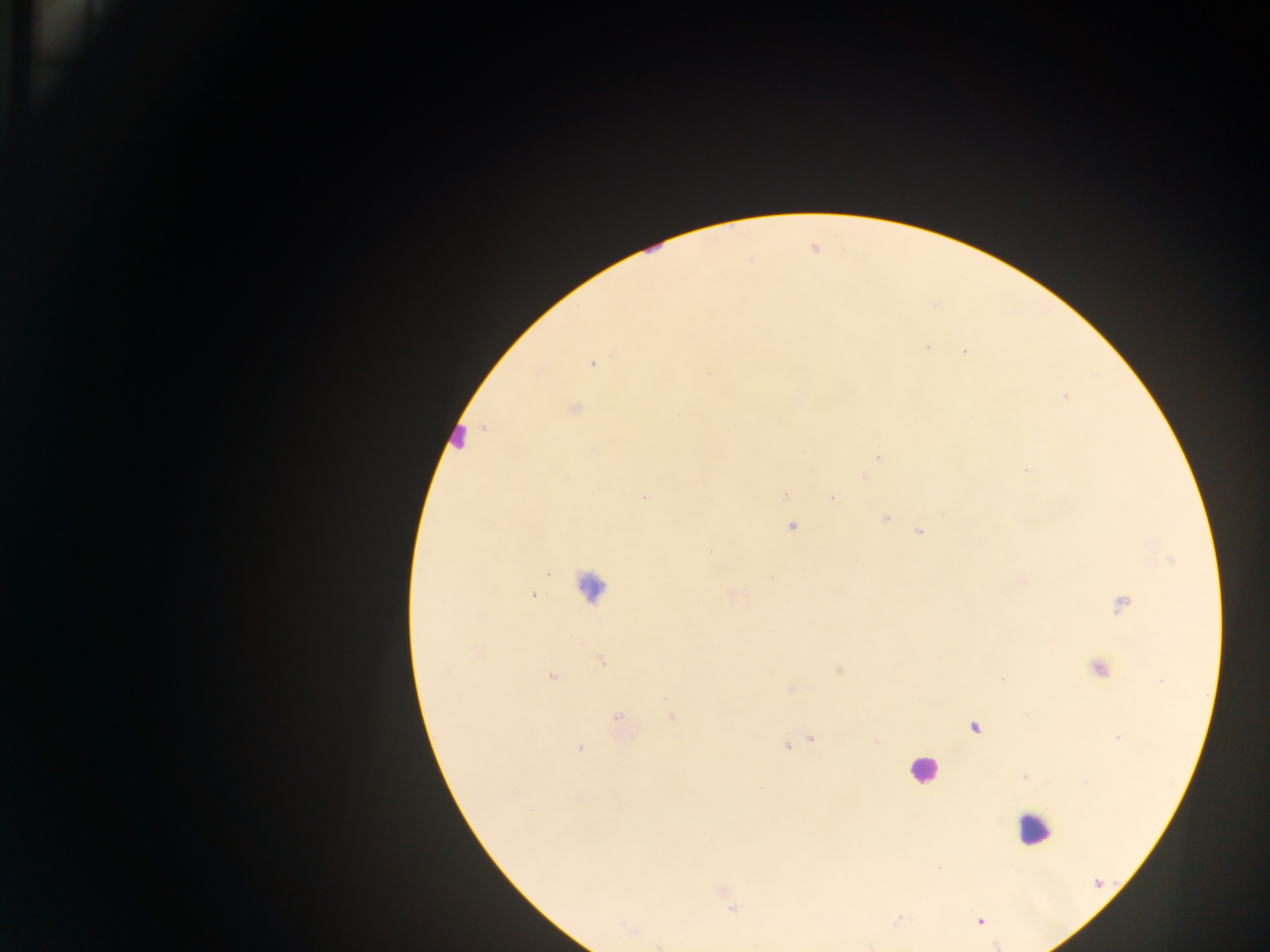

Approximate centers as {x, y} in pixels. Malaria parasite locations: {926, 347}, {965, 351}, {593, 364}, {709, 375}, {1065, 395}, {573, 409}, {878, 455}, {1026, 469}, {864, 476}, {785, 494}, {644, 497}, {832, 497}, {884, 517}, {791, 526}, {919, 531}, {547, 572}, {771, 577}, {533, 595}, {1121, 604}, {602, 661}, {1097, 668}, {837, 670}, {550, 676}, {1001, 678}, {790, 689}, {617, 718}, {671, 718}, {973, 727}, {812, 738}, {1118, 738}, {876, 741}, {786, 746}, {579, 748}, {1025, 775}, {939, 867}, {724, 894}, {732, 906}, {898, 917}, {979, 921}, {995, 945}. Leukocyte locations: {458, 438}, {590, 586}, {923, 770}, {1033, 829}. Thick blood film. Single field of view. Image is 1270×952 pixels. Collected in Ghana. Photographed through a microscope with a mobile-phone camera.